Describe the morphology of the erythrocytes.
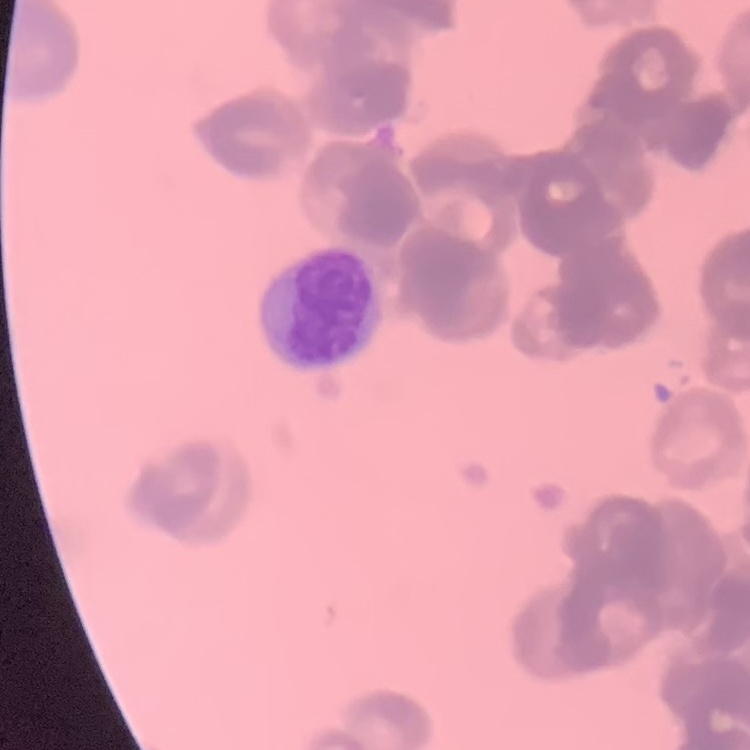
Rouleaux formation.

Summary:
  - Stain: Field's or Giemsa
  - Preparation: thin blood film
  - Image type: one tile cut from a larger photomicrograph